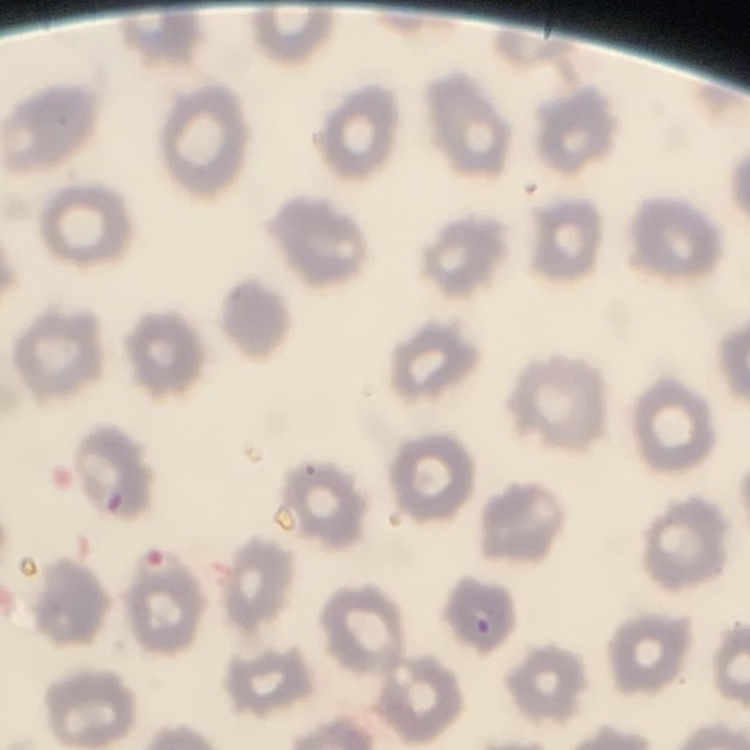

The erythrocytes show no rouleaux formation. Stained with either Field's or Giemsa. One tile cut from a larger photomicrograph. Thin peripheral smear.